Report the malaria status of this cell.
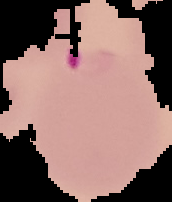
It is parasitized.

Summary:
  - Image type: cell region segmented out of the field of view; surrounding area masked to black
  - Preparation: thin blood film
  - Image size: 172×202 pixels